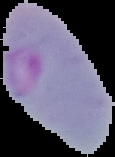
Summary:
  - Image type: cell region segmented out of the field of view; surrounding area masked to black
  - Image size: 115×157 pixels
  - Result: Plasmodium parasites detected
  - Preparation: thin blood film